Classify this cell by malaria status.
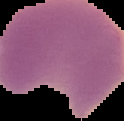

Parasitized.

Image is 124×121 pixels. Cell region segmented out of the field of view; the surrounding area is masked to black. From a thin blood film.